Report the malaria status of this cell.
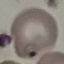
Parasitized.

Summary:
  - Capture: smartphone camera at the microscope eyepiece
  - Stain: Giemsa
  - Preparation: thin blood smear
  - Image type: cell patch, automatically extracted from a larger field of view and resized to 64 × 64 pixels